Name the parasite shown.
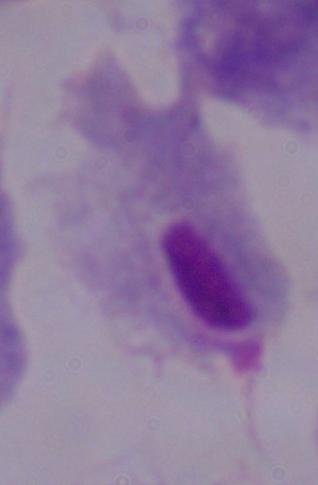

This is a trichomonad.

magnification: 1000x
modality: micrograph